Draw a bounding box around every leukocyte (white blood cell).
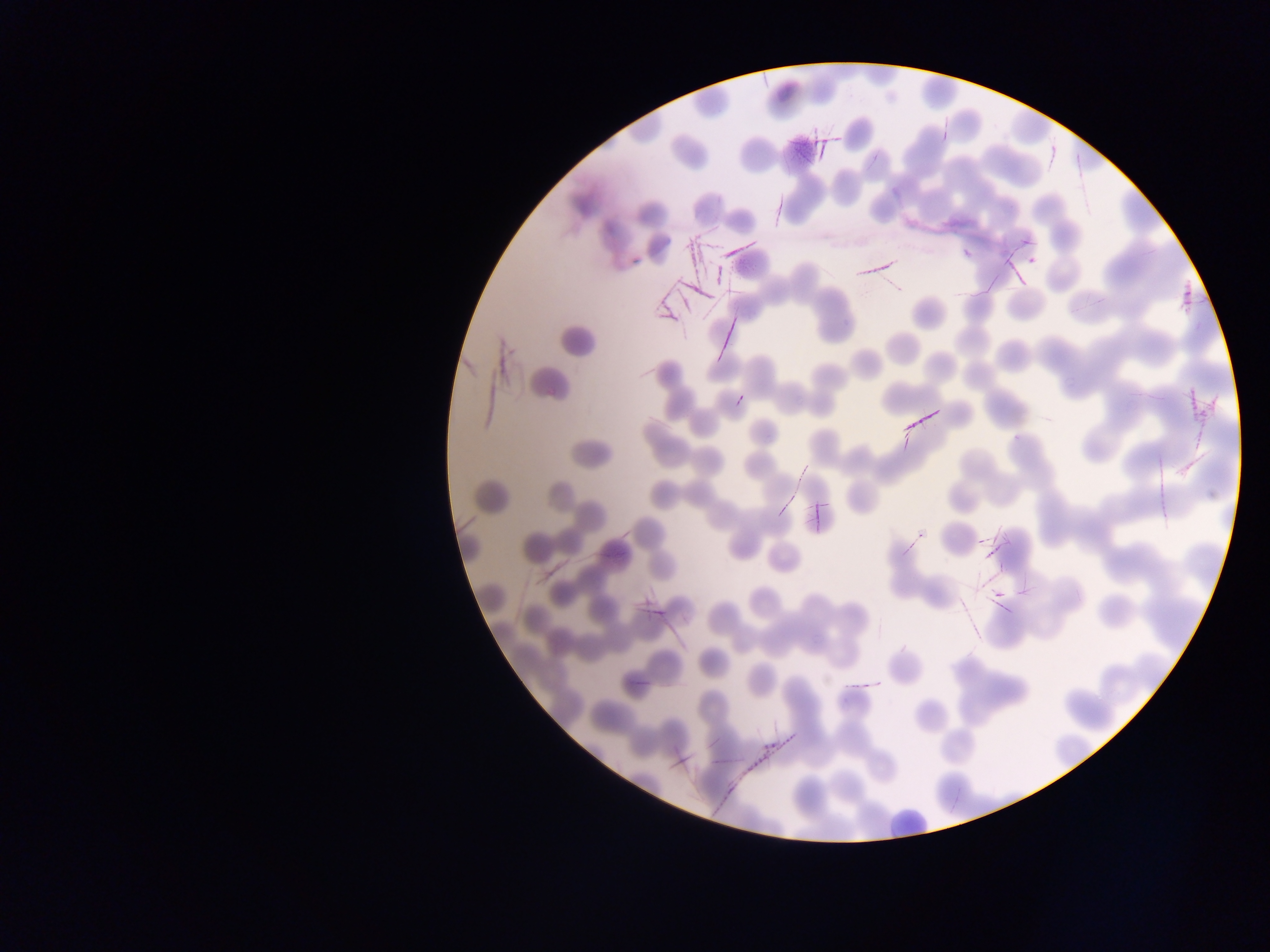
Approximate bounding boxes as (left, top, right, bottom) in pixels.
Leukocytes: (885, 785, 935, 833).

Summary:
  - Artifact (stain precipitate or debris) locations: (800, 134, 845, 160), (647, 226, 721, 324), (847, 228, 888, 292), (982, 233, 1045, 283), (708, 238, 774, 259), (460, 301, 506, 441), (714, 311, 744, 367), (1149, 370, 1200, 484), (901, 387, 954, 440), (772, 458, 807, 509), (961, 519, 992, 621), (635, 560, 686, 628), (724, 679, 800, 788)
  - Field of view: single
  - Country: Ghana
  - Preparation: thin blood smear
  - Image size: 1270×952 pixels
  - Capture: mobile-phone photograph through a microscope